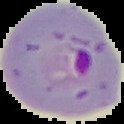 Image is 124×124 pixels. The area outside the segmented cell region is set to black. Malaria status: parasitized. From a thin blood film.